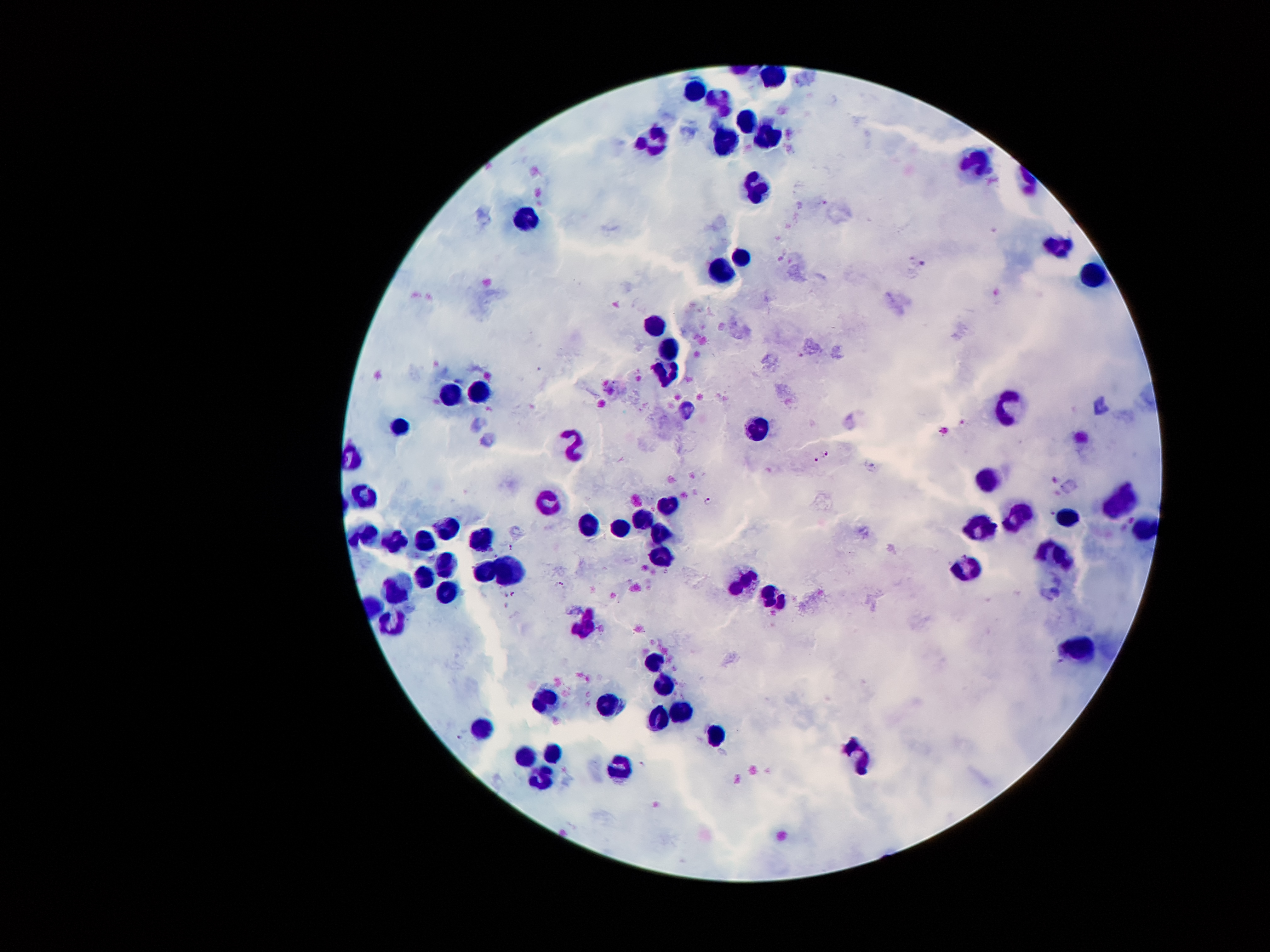
coordinate format = approximate centers as (x, y) in pixels
malaria parasite locations = (802, 356), (826, 453), (816, 459), (710, 500), (1053, 513), (510, 548), (560, 585), (513, 594), (1061, 661), (459, 737), (642, 763)
leukocyte locations = (769, 75), (694, 90), (718, 99), (749, 121), (770, 133), (654, 139), (724, 141), (975, 160), (758, 189), (524, 217), (1057, 246), (742, 255), (725, 272), (1095, 276), (654, 324), (670, 346), (667, 373), (481, 389), (452, 393), (1005, 406), (396, 430), (758, 430), (574, 440), (988, 480), (363, 493), (548, 498), (1117, 501), (667, 503), (1020, 514), (1068, 516), (643, 519), (585, 526), (977, 526), (621, 528), (443, 529), (1138, 530), (367, 533), (658, 533), (483, 537), (398, 540), (425, 540), (660, 551), (1057, 551), (445, 561), (484, 570), (963, 570), (422, 575), (506, 575), (745, 581), (398, 588), (445, 589), (771, 596), (391, 619), (587, 627), (1080, 648), (653, 661), (664, 684), (545, 700), (606, 707), (683, 712), (657, 718), (484, 722), (716, 733), (554, 752), (522, 754), (859, 758), (620, 768), (541, 781)
magnification = 100x
capture = smartphone camera through the microscope eyepiece
preparation = thick peripheral-blood smear
field of view = single
image size = 1270×952 pixels
stain = Giemsa
patient malaria status = infected with Plasmodium falciparum